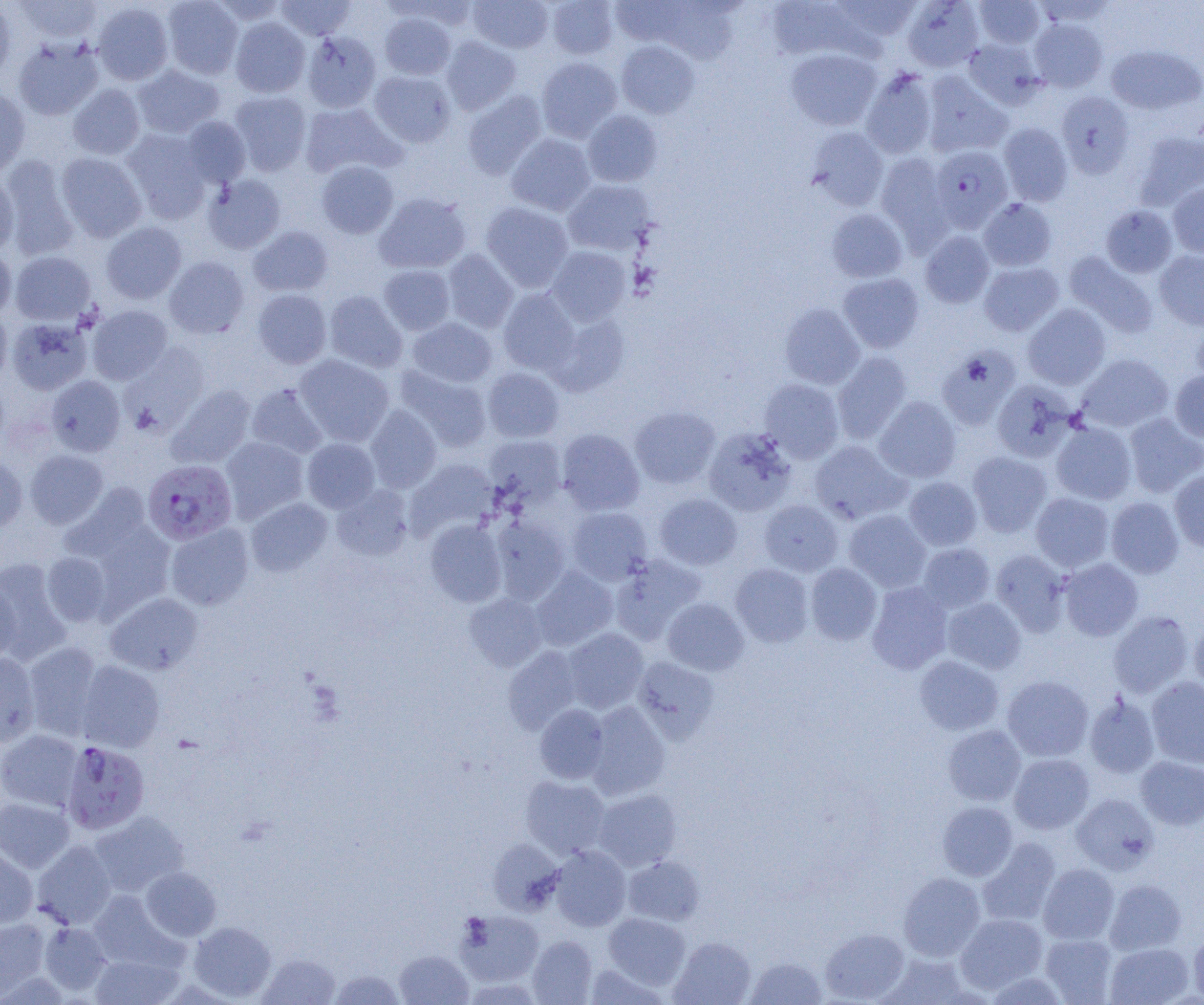 Approximate bounding boxes as [x1, y1, x2, y2] in pixels. Plasmodium falciparum-infected red blood cell locations: [929, 145, 1013, 233], [143, 459, 237, 545], [61, 740, 150, 835]. Uninfected red blood cell locations: [15, 0, 103, 43], [162, 0, 243, 79], [208, 0, 288, 25], [276, 0, 355, 41], [388, 0, 481, 31], [468, 0, 553, 53], [548, 0, 618, 59], [611, 0, 689, 47], [764, 0, 869, 62], [832, 0, 922, 42], [902, 0, 984, 72], [973, 0, 1045, 49], [0, 2, 15, 84], [92, 2, 174, 85], [658, 2, 741, 64], [379, 11, 456, 80], [230, 17, 310, 97], [1029, 18, 1108, 92], [302, 31, 381, 113], [441, 36, 521, 115], [13, 37, 104, 120], [963, 38, 1044, 108], [616, 40, 700, 118], [1107, 45, 1204, 115], [786, 48, 882, 130], [536, 57, 622, 142], [132, 64, 225, 139], [860, 68, 938, 159], [369, 70, 456, 147], [921, 71, 1012, 157], [68, 84, 146, 160], [229, 90, 312, 175], [462, 90, 548, 179], [0, 91, 31, 177], [1057, 91, 1134, 177], [300, 102, 403, 179], [582, 110, 663, 187], [181, 116, 251, 187], [998, 122, 1073, 206], [807, 126, 889, 211], [122, 129, 211, 222], [1133, 131, 1204, 210], [506, 133, 596, 216], [56, 152, 147, 242], [876, 152, 953, 248], [2, 156, 79, 259], [316, 161, 399, 238], [0, 173, 19, 255], [203, 174, 286, 254], [562, 179, 656, 255], [1168, 182, 1204, 257], [374, 192, 472, 274], [978, 198, 1057, 271], [481, 202, 574, 291], [1101, 205, 1177, 277], [826, 208, 908, 282], [101, 222, 186, 303], [248, 225, 333, 297], [920, 231, 995, 308], [0, 246, 17, 320], [546, 246, 631, 325], [442, 249, 519, 333], [1155, 250, 1204, 330], [11, 251, 95, 324], [1063, 251, 1158, 338], [165, 256, 249, 338], [979, 262, 1063, 336], [379, 265, 455, 335], [838, 273, 924, 353], [498, 288, 579, 375], [253, 289, 332, 368], [324, 291, 407, 372], [779, 302, 865, 389], [1023, 304, 1111, 390], [87, 305, 172, 384], [0, 307, 11, 387], [548, 311, 630, 396], [7, 316, 93, 394], [408, 317, 497, 387], [1192, 318, 1204, 389], [121, 343, 210, 434], [936, 346, 1020, 429], [832, 352, 912, 444], [295, 354, 394, 446], [1077, 354, 1173, 433], [395, 365, 493, 452], [483, 367, 564, 442], [1169, 370, 1204, 442], [46, 375, 125, 456], [759, 378, 844, 464], [992, 379, 1078, 462], [0, 380, 10, 450], [245, 383, 328, 459], [167, 384, 256, 468], [874, 396, 961, 483], [365, 405, 442, 492], [629, 405, 720, 489], [1123, 413, 1204, 497], [1051, 421, 1137, 504], [703, 427, 796, 516], [556, 428, 644, 515], [484, 435, 566, 507], [221, 437, 308, 522], [302, 438, 380, 512], [809, 440, 910, 524], [25, 450, 108, 528], [968, 452, 1052, 537], [0, 455, 27, 531], [406, 458, 499, 540], [1169, 469, 1204, 551], [904, 476, 982, 550], [60, 483, 152, 563], [332, 484, 413, 561], [654, 493, 742, 570], [1031, 493, 1114, 572], [246, 497, 332, 576], [1106, 497, 1183, 578], [760, 500, 843, 576], [567, 506, 653, 585], [844, 510, 931, 592], [490, 516, 570, 604], [82, 519, 176, 616], [425, 519, 507, 607], [166, 523, 253, 610], [917, 543, 995, 613], [991, 549, 1070, 636], [41, 552, 112, 626], [609, 555, 706, 644], [0, 558, 71, 662], [1059, 558, 1143, 641], [806, 563, 882, 645], [730, 564, 814, 647], [531, 566, 618, 651], [0, 577, 21, 662], [867, 582, 952, 674], [105, 591, 203, 675], [464, 592, 547, 672], [663, 597, 749, 676], [942, 598, 1026, 674], [1109, 611, 1193, 698], [1189, 614, 1204, 694], [563, 628, 648, 713], [23, 641, 105, 740], [503, 646, 584, 733], [0, 651, 40, 748], [914, 655, 1004, 735], [633, 657, 719, 743], [77, 660, 165, 752], [1002, 675, 1093, 761], [1146, 677, 1204, 769], [1084, 693, 1160, 778], [586, 701, 671, 800], [534, 704, 609, 783], [942, 724, 1026, 806], [0, 729, 83, 811], [1009, 754, 1094, 834], [1136, 756, 1204, 830], [520, 776, 610, 858], [593, 789, 682, 871], [1072, 793, 1159, 875], [0, 797, 75, 872], [937, 801, 1017, 881], [89, 811, 189, 897], [977, 838, 1061, 928], [488, 839, 564, 915], [32, 840, 117, 929], [0, 844, 38, 929], [550, 846, 630, 931], [624, 856, 704, 926], [1038, 864, 1119, 944], [140, 867, 221, 941], [899, 873, 985, 960], [1105, 879, 1186, 954], [86, 890, 182, 970], [456, 910, 544, 986], [603, 913, 690, 988], [955, 913, 1047, 993], [0, 917, 49, 998], [39, 921, 112, 995], [188, 921, 276, 1001], [820, 928, 909, 1003], [1189, 929, 1204, 1002], [1040, 933, 1118, 1004], [528, 935, 597, 1004], [670, 937, 756, 1005], [1105, 942, 1194, 1005], [395, 950, 473, 1005], [90, 951, 183, 1005], [258, 953, 341, 1005], [878, 953, 970, 1004], [746, 955, 826, 1004], [584, 962, 668, 1004], [328, 969, 405, 1004], [984, 971, 1070, 1004]. Slide-level diagnosis: Plasmodium falciparum. Thin blood film. Optical microscopy. Single field of view. Image is 1204×1005 pixels. 1000x magnification.